Give the position of every Plasmodium parasite.
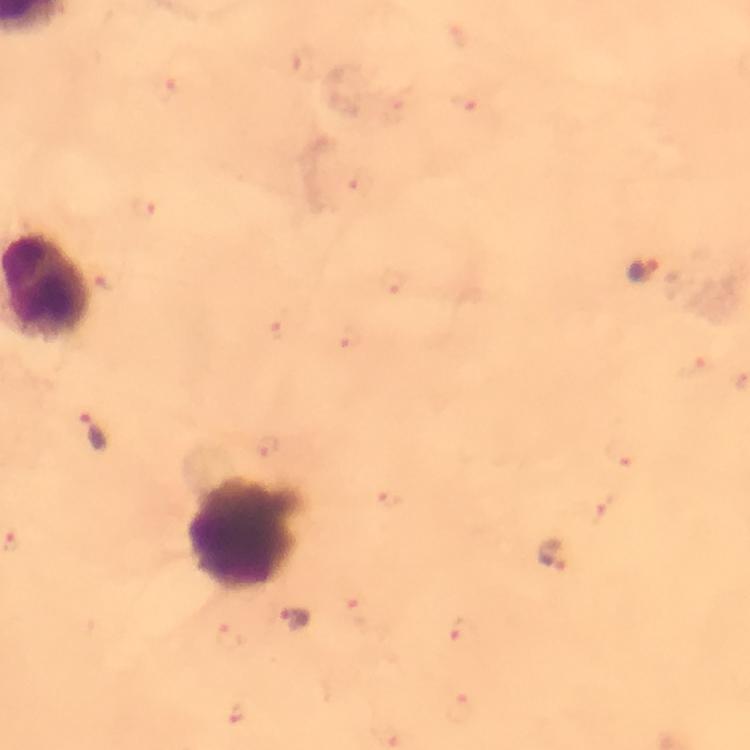

Approximate object centers, in pixels from the top-left corner.
Plasmodium parasites: (x=642, y=269), (x=95, y=433), (x=552, y=555), (x=295, y=620).

Thick blood film. 100x magnification. From a malaria diagnostic workup. A crop from one field of view. Immersion oil applied. Image is 750×750 pixels. Giemsa-stained preparation. Smartphone photograph taken through a microscope.